Classify this cell by malaria status.
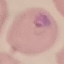
It is parasitized.

{
  "capture": "smartphone through the microscope eyepiece",
  "stain": "Giemsa",
  "image_type": "automatically extracted cell patch, resized to 64 × 64 pixels",
  "preparation": "thin blood film"
}